Locate every leukocyte (white blood cell).
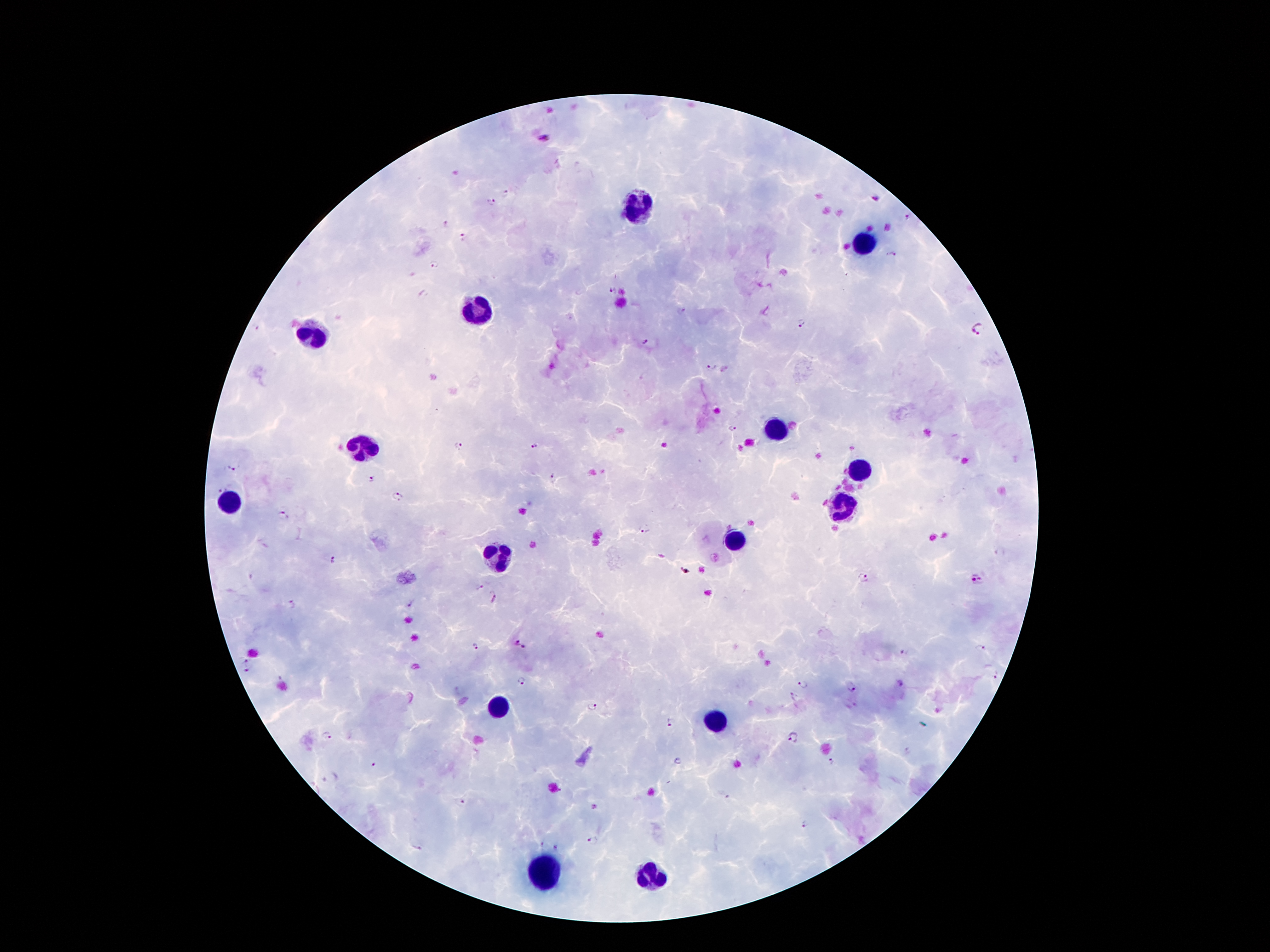

Approximate object centers, in pixels from the top-left corner.
Leukocytes: (x=639, y=208), (x=863, y=244), (x=476, y=307), (x=313, y=336), (x=775, y=431), (x=361, y=450), (x=858, y=472), (x=228, y=504), (x=842, y=512), (x=735, y=542), (x=497, y=561), (x=501, y=709), (x=718, y=721), (x=541, y=868), (x=651, y=874).

{
  "capture": "smartphone through the microscope eyepiece",
  "magnification": "100x",
  "field_of_view": "one from this slide",
  "plasmodium_parasite_locations": "approximate object centers, in pixels from the top-left corner: (x=542, y=139), (x=506, y=192), (x=875, y=198), (x=492, y=202), (x=907, y=216), (x=446, y=225), (x=461, y=238), (x=891, y=255), (x=435, y=265), (x=612, y=290), (x=423, y=293), (x=680, y=311), (x=804, y=324), (x=979, y=328), (x=646, y=342), (x=713, y=370), (x=732, y=429), (x=460, y=446), (x=534, y=446), (x=235, y=466), (x=556, y=477), (x=371, y=478), (x=218, y=489), (x=397, y=496), (x=285, y=514), (x=644, y=527), (x=333, y=560), (x=866, y=578), (x=977, y=580), (x=479, y=588), (x=494, y=597), (x=292, y=604), (x=409, y=604), (x=519, y=645), (x=981, y=646), (x=476, y=649), (x=906, y=651), (x=245, y=659), (x=247, y=671), (x=997, y=676), (x=522, y=681), (x=899, y=682), (x=802, y=685), (x=852, y=687), (x=591, y=707), (x=671, y=723), (x=327, y=736), (x=793, y=738), (x=832, y=763), (x=373, y=765), (x=329, y=778), (x=461, y=802), (x=806, y=825), (x=593, y=841), (x=556, y=847), (x=417, y=848)",
  "patient_malaria_status": "infected with Plasmodium falciparum",
  "preparation": "thick blood film",
  "stain": "Giemsa",
  "image_size": "1270×952 pixels"
}